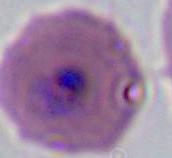

modality = micrograph
identification = Plasmodium
magnification = 400x or 1000x